Assess the morphology of the erythrocytes.
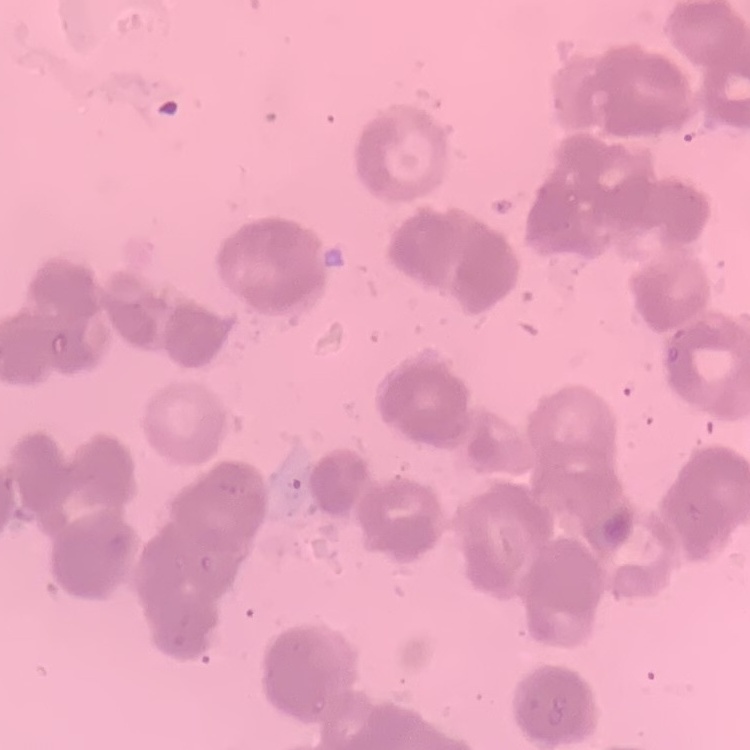
They show rouleaux formation.

image type = one tile cut from a larger photomicrograph
preparation = thin blood smear
stain = Field's or Giemsa